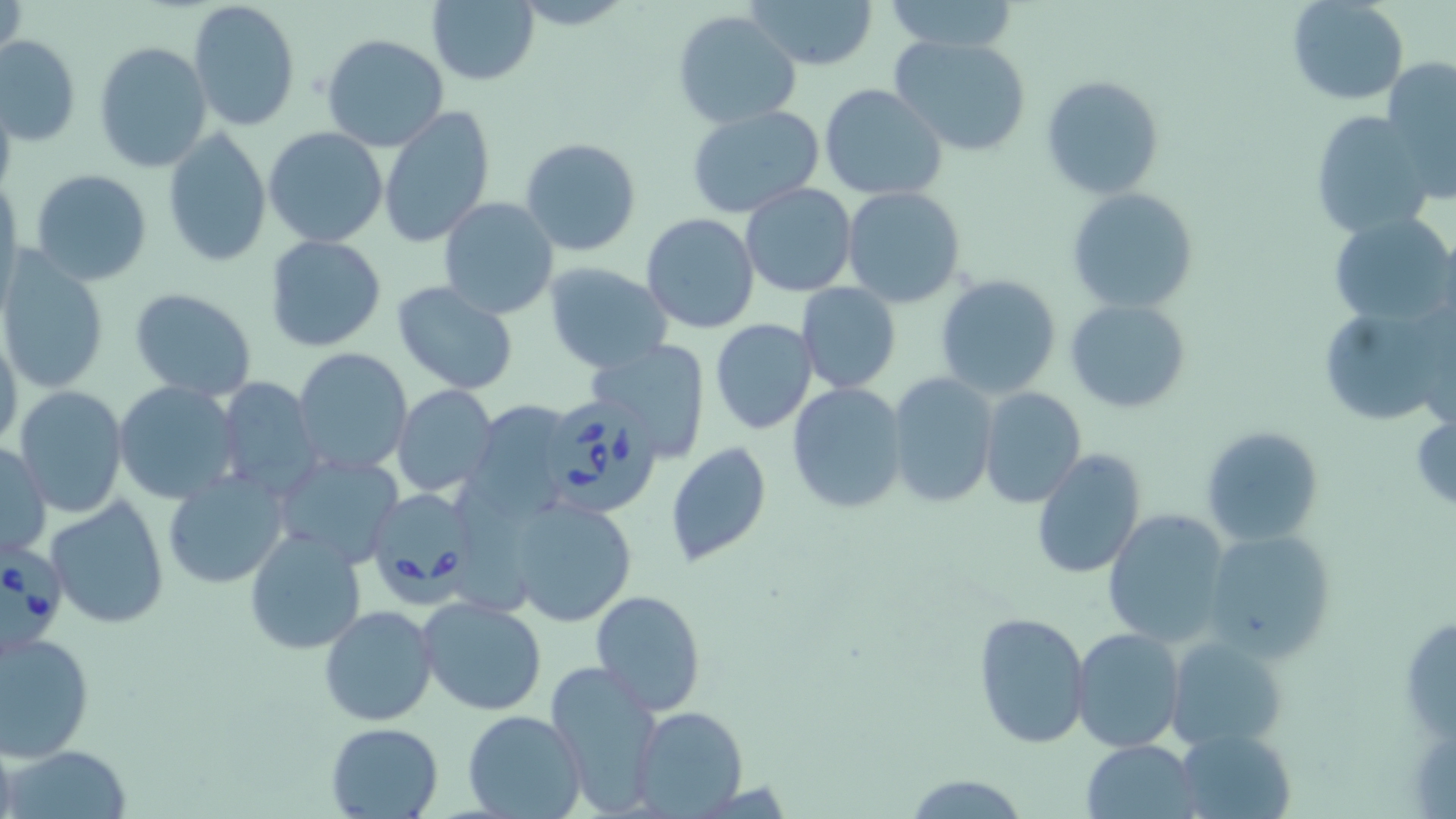

slide-level diagnosis = Babesia divergens
stain = May-Grünwald-Giemsa
preparation = thin blood film
uninfected red blood cell locations = approximate bounding boxes as (x1,y1)-(x2,y2) corner pairs in pixels: (2,0)-(27,73), (427,0)-(539,85), (749,0)-(877,71), (886,0)-(1020,54), (1287,0)-(1408,105), (187,1)-(301,134), (673,9)-(801,129), (322,34)-(451,153), (888,34)-(1032,157), (1,36)-(81,147), (94,41)-(213,172), (1384,57)-(1456,201), (1041,74)-(1165,198), (820,84)-(947,201), (0,91)-(17,198), (686,104)-(824,217), (377,105)-(497,248), (1307,114)-(1434,237), (262,126)-(389,248), (160,129)-(272,267), (519,137)-(641,257), (30,168)-(154,286), (739,183)-(856,298), (842,187)-(966,309), (1066,187)-(1201,313), (438,198)-(558,319), (1329,212)-(1454,329), (642,213)-(759,333), (263,235)-(387,354), (1,255)-(109,394), (542,264)-(671,375), (936,274)-(1062,398), (390,280)-(517,393), (795,284)-(901,394), (129,288)-(258,401), (1065,298)-(1191,414), (1314,302)-(1449,427), (710,319)-(819,435), (0,329)-(23,454), (588,341)-(711,459), (293,347)-(413,477), (886,371)-(998,509), (210,375)-(321,498), (113,380)-(242,503), (787,381)-(909,516), (14,385)-(126,520), (392,385)-(498,496), (978,386)-(1086,510), (466,400)-(581,514), (1411,408)-(1456,515), (1201,425)-(1325,546), (1,440)-(50,561), (665,442)-(772,567), (1031,448)-(1144,581), (273,451)-(406,568), (163,470)-(288,590), (44,497)-(168,629), (509,497)-(637,626), (1102,509)-(1233,646), (245,528)-(366,655), (1201,528)-(1337,662), (590,589)-(706,715), (418,596)-(547,716), (319,604)-(439,726), (973,611)-(1090,747), (1070,627)-(1186,753), (1,629)-(95,761), (1168,636)-(1287,749), (545,659)-(664,814), (632,706)-(747,816), (463,710)-(585,819), (325,721)-(446,817), (1175,726)-(1297,818), (1083,739)-(1198,817), (6,744)-(134,818), (903,773)-(1031,817)
field of view = one of a larger specimen
magnification = 1000x
Babesia divergens-infected red blood cell locations = approximate bounding boxes as (x1,y1)-(x2,y2) corner pairs in pixels: (540,395)-(661,518), (368,488)-(480,598), (0,540)-(64,648)
modality = light microscopy
image size = 1456×819 pixels